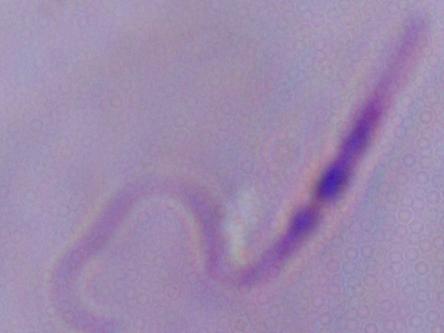

{
  "modality": "photomicrograph",
  "magnification": "1000x",
  "identification": "Leishmania"
}